State the blood parasite species.
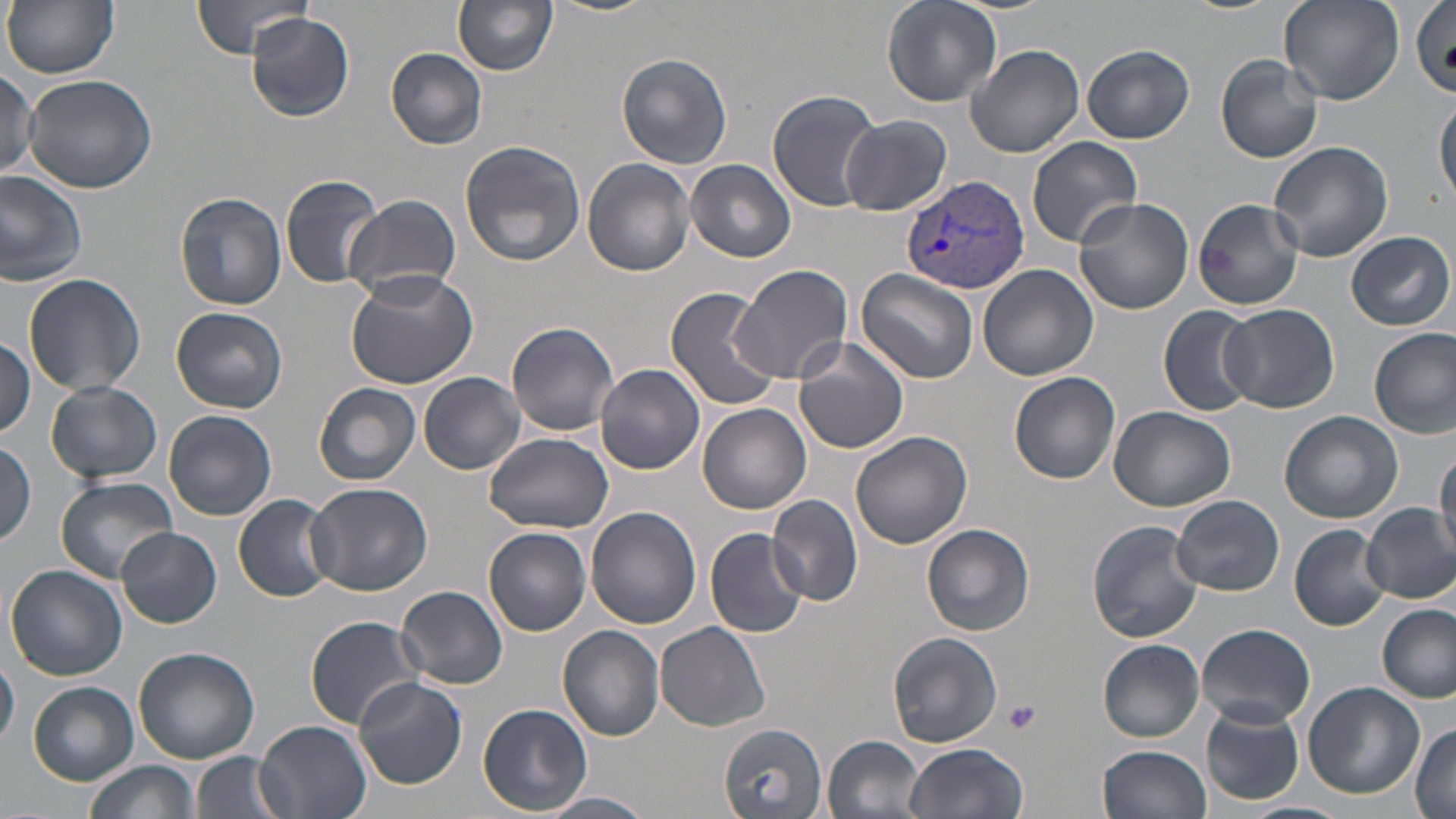
Plasmodium vivax.

Summary:
  - Coordinate format: approximate bounding boxes as (x1, y1, x2, y2) in pixels
  - Plasmodium vivax-infected red blood cell locations: (901, 174, 1030, 295)
  - Uninfected red blood cell locations: (5, 0, 119, 79), (190, 0, 315, 59), (549, 0, 661, 18), (883, 0, 1002, 108), (1178, 0, 1280, 14), (1281, 0, 1403, 105), (1410, 0, 1455, 99), (454, 1, 558, 75), (244, 12, 356, 122), (967, 44, 1086, 159), (1082, 44, 1196, 143), (386, 48, 488, 148), (617, 52, 734, 170), (1216, 56, 1322, 163), (2, 69, 41, 179), (24, 73, 156, 193), (766, 90, 882, 211), (1435, 92, 1456, 205), (840, 116, 952, 216), (1027, 135, 1142, 247), (458, 138, 587, 267), (1268, 141, 1393, 262), (584, 158, 696, 277), (686, 158, 796, 262), (0, 169, 87, 286), (281, 174, 386, 289), (175, 191, 288, 313), (342, 192, 462, 301), (1074, 197, 1195, 315), (1193, 199, 1304, 312), (1347, 231, 1453, 331), (731, 262, 852, 386), (342, 265, 477, 389), (978, 266, 1099, 382), (856, 268, 981, 384), (22, 274, 145, 396), (664, 287, 779, 411), (1220, 303, 1339, 413), (1159, 305, 1262, 419), (171, 306, 289, 413), (507, 320, 621, 435), (1370, 327, 1455, 438), (0, 337, 35, 438), (793, 339, 910, 454), (597, 363, 705, 474), (419, 371, 525, 474), (1011, 371, 1120, 483), (46, 380, 162, 485), (315, 382, 421, 485), (698, 403, 810, 512), (1109, 404, 1237, 510), (164, 410, 277, 521), (1279, 411, 1403, 524), (851, 431, 972, 550), (484, 432, 615, 532), (0, 438, 38, 545), (1433, 447, 1456, 557), (56, 476, 179, 583), (306, 482, 435, 597), (233, 495, 336, 601), (766, 495, 863, 605), (1172, 495, 1284, 596), (1361, 504, 1456, 604), (586, 506, 701, 629), (1086, 520, 1206, 643), (922, 523, 1034, 637), (1291, 525, 1388, 630), (115, 527, 221, 628), (484, 527, 591, 635), (705, 527, 809, 639), (5, 564, 127, 681), (394, 585, 508, 690), (1377, 604, 1454, 703), (303, 615, 425, 730), (656, 622, 771, 730), (1198, 622, 1315, 728), (559, 625, 664, 742), (885, 631, 1003, 749), (1098, 639, 1205, 741), (133, 647, 259, 764), (0, 650, 20, 748), (352, 675, 468, 788), (28, 682, 139, 785), (1303, 682, 1425, 799), (479, 704, 591, 814), (1370, 704, 1456, 815), (1202, 705, 1304, 807), (255, 721, 370, 819), (1411, 722, 1455, 819), (718, 723, 828, 816), (824, 735, 928, 819), (903, 743, 1028, 819), (1097, 744, 1212, 819), (191, 751, 291, 819), (84, 759, 199, 819), (545, 792, 651, 818), (1239, 802, 1355, 819)
  - Platelet locations: (1001, 700, 1041, 735)
  - Modality: light microscopy
  - Field of view: one of a larger specimen
  - Image size: 1456×819 pixels
  - Magnification: 1000x
  - Stain: May-Grünwald-Giemsa
  - Preparation: thin blood smear